Locate every Plasmodium falciparum-infected red blood cell.
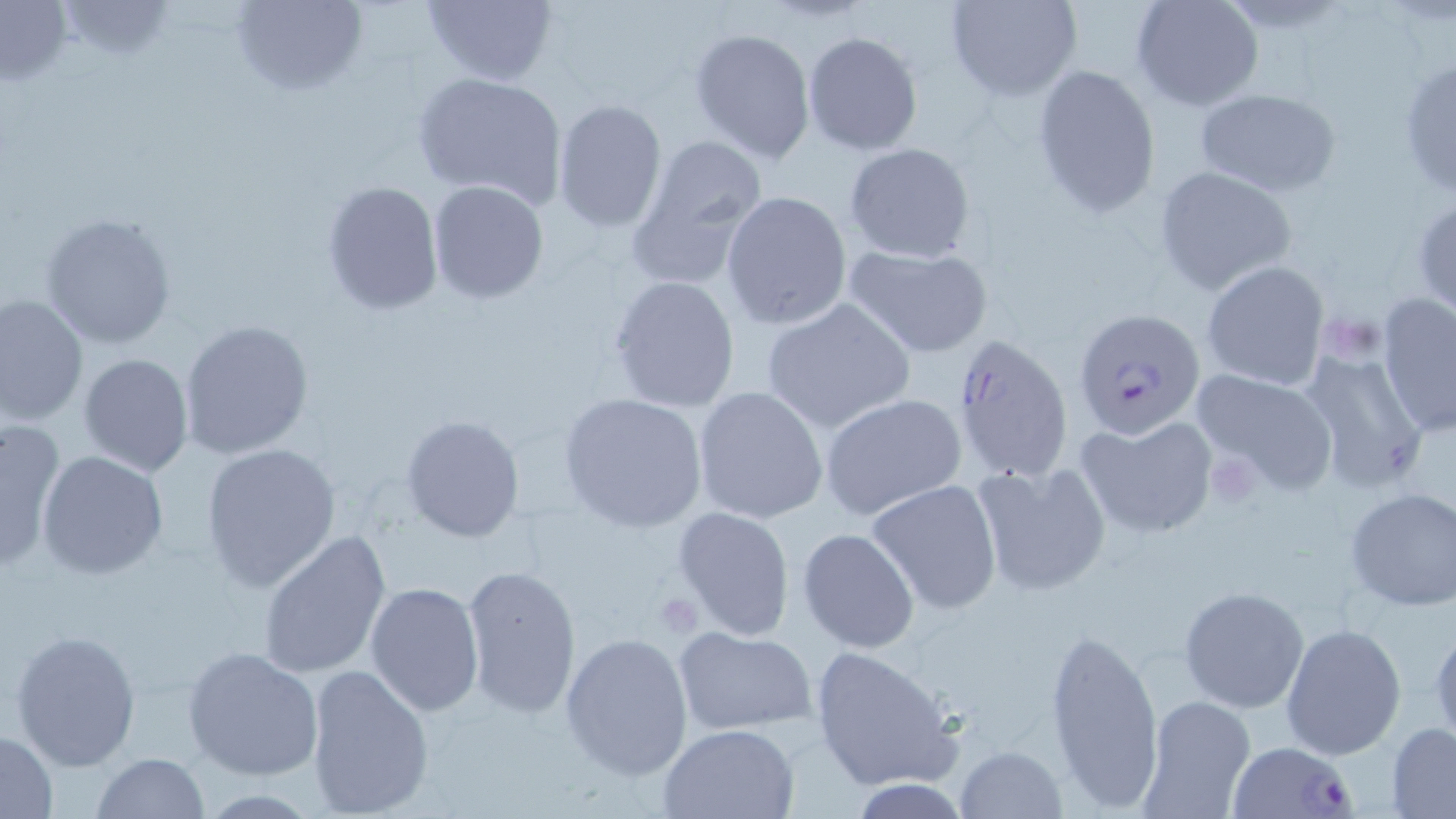

Approximate bounding boxes as (x1, y1, x2, y2) in pixels.
Plasmodium falciparum-infected red blood cells: (1074, 308, 1208, 440), (948, 334, 1076, 485), (1227, 739, 1360, 819).

Summary:
  - Platelet locations: (1336, 321, 1386, 358), (1210, 461, 1260, 506), (654, 591, 703, 636)
  - Uninfected red blood cell locations: (228, 0, 367, 98), (421, 0, 559, 88), (945, 0, 1081, 101), (1130, 0, 1263, 112), (55, 1, 182, 60), (0, 2, 73, 88), (689, 27, 815, 163), (802, 31, 922, 155), (1396, 58, 1456, 201), (1031, 63, 1162, 218), (413, 71, 569, 208), (1194, 88, 1340, 197), (552, 98, 667, 232), (622, 133, 771, 289), (844, 143, 976, 264), (1155, 164, 1299, 296), (320, 180, 445, 315), (427, 181, 550, 303), (720, 190, 853, 330), (1412, 194, 1456, 316), (39, 211, 178, 350), (841, 242, 995, 358), (1201, 260, 1329, 392), (607, 274, 741, 413), (0, 293, 88, 427), (1378, 295, 1456, 437), (761, 298, 916, 436), (177, 318, 313, 459), (1297, 347, 1432, 493), (78, 353, 194, 476), (1190, 369, 1338, 496), (692, 386, 829, 525), (558, 393, 708, 531), (819, 394, 967, 522), (398, 415, 524, 544), (1074, 415, 1218, 538), (0, 422, 67, 568), (201, 442, 341, 593), (36, 449, 168, 580), (971, 458, 1112, 597), (868, 478, 1003, 614), (1343, 488, 1456, 610), (673, 506, 794, 638), (797, 528, 920, 653), (258, 529, 391, 679), (462, 562, 582, 716), (365, 583, 485, 717), (1178, 586, 1310, 713), (1429, 617, 1456, 748), (1280, 623, 1406, 762), (672, 626, 819, 738), (1047, 626, 1164, 810), (9, 630, 141, 771), (560, 632, 693, 779), (182, 645, 325, 781), (807, 646, 962, 793), (304, 662, 435, 818), (1136, 695, 1257, 818), (1387, 723, 1456, 816), (659, 724, 799, 818), (1, 730, 58, 816), (955, 745, 1065, 818), (90, 752, 212, 818), (195, 789, 320, 817)
  - Slide-level diagnosis: Plasmodium falciparum
  - Field of view: one of a larger specimen
  - Magnification: 1000x
  - Image size: 1456×819 pixels
  - Modality: optical microscopy
  - Stain: May-Grünwald-Giemsa
  - Preparation: thin blood film